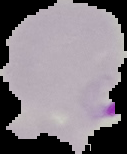

Summary:
  - Image size: 127×154 pixels
  - Image type: segmented cell region on a black background
  - Result: Plasmodium parasites detected
  - Preparation: thin blood film